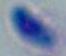

Photomicrograph. 1000x magnification. Toxoplasma gondii is shown.